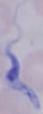

A trypanosome is seen. 1000x magnification. Micrograph.